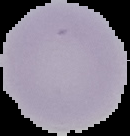
image size = 130×136 pixels
preparation = thin blood smear
malaria status = uninfected
image type = cell region segmented out of the field of view; surrounding area masked to black